Report the malaria status of this cell.
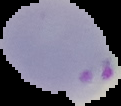

Parasitized.

image type = cell region segmented out of the field of view; surrounding area masked to black
preparation = thin blood film
image size = 121×106 pixels